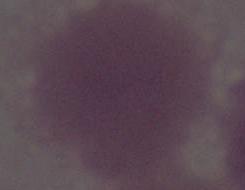

modality = photomicrograph
magnification = 1000x
identification = erythrocyte